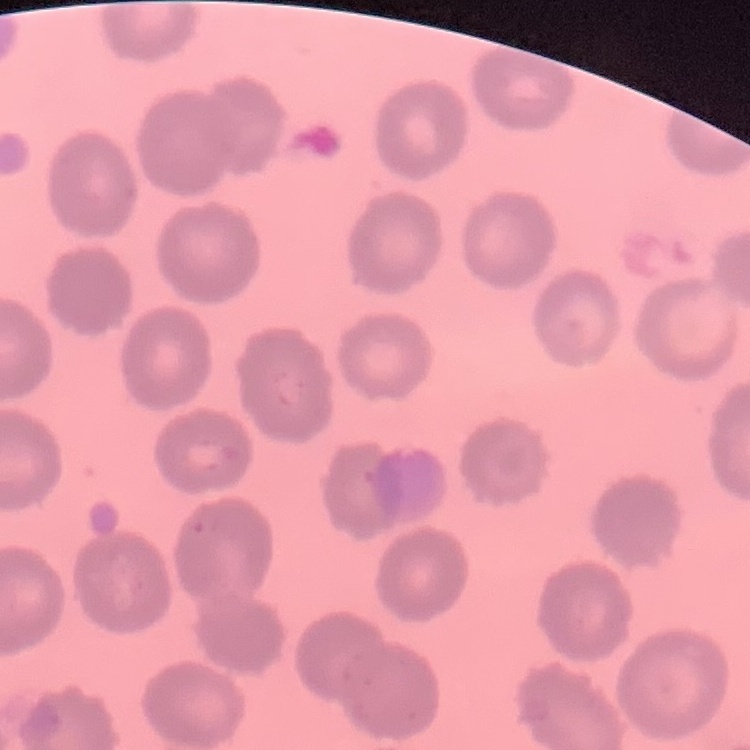

Summary:
  - Erythrocyte morphology: no rouleaux formation
  - Image type: one tile cut from a larger photomicrograph
  - Preparation: thin blood smear
  - Stain: Field's or Giemsa